Locate and identify every blood parasite.
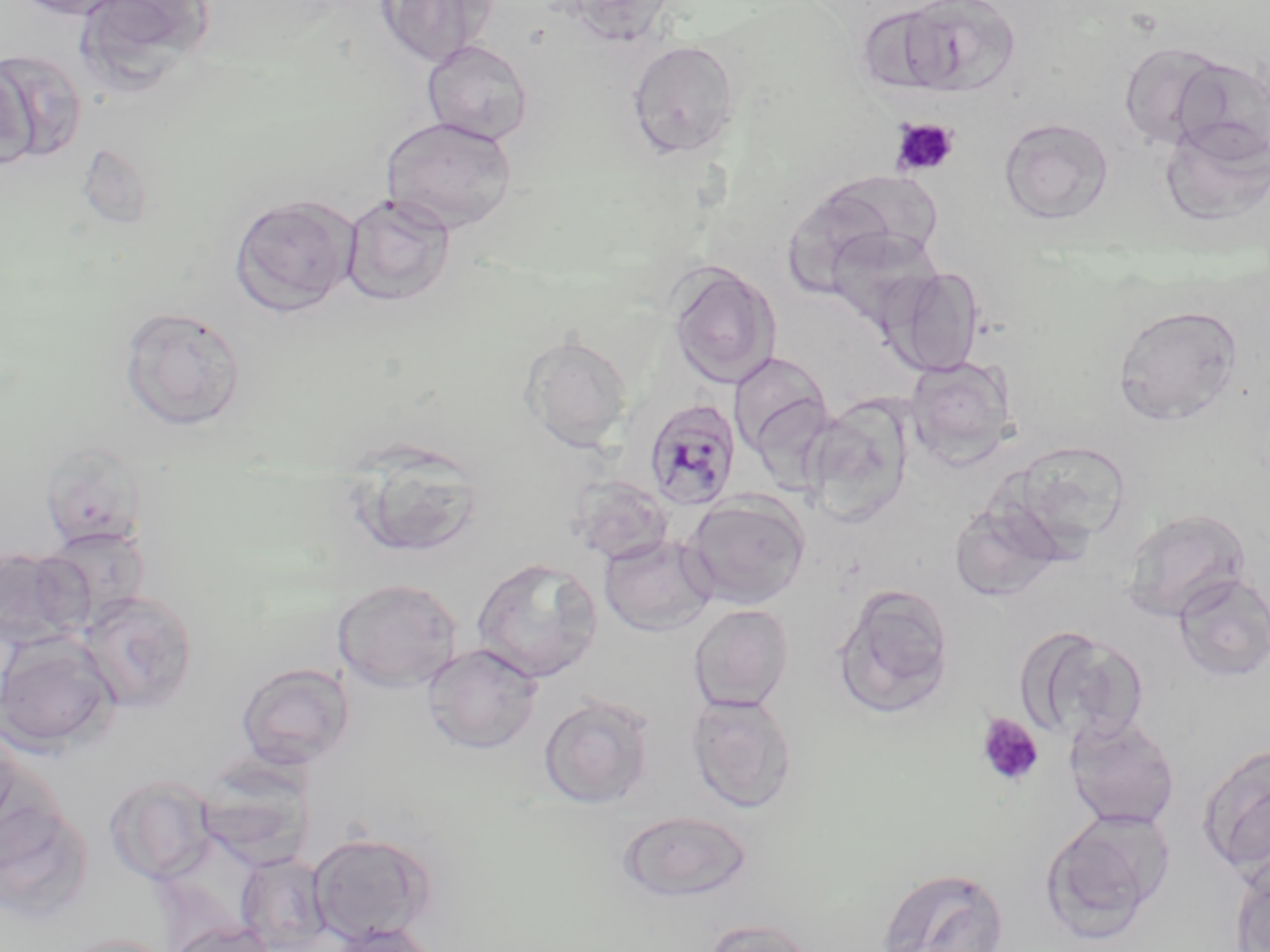
Approximate bounding boxes as [x1, y1, x2, y2] in pixels.
Plasmodium malariae-infected red blood cells: [642, 397, 742, 511].
No Plasmodium falciparum, Plasmodium ovale, Plasmodium vivax, Babesia divergens, or Trypanosoma brucei observed.

Summary:
  - Platelet locations: [891, 118, 959, 177], [976, 714, 1044, 787]
  - Uninfected red blood cell locations: [10, 0, 137, 20], [73, 0, 215, 92], [376, 0, 499, 68], [558, 0, 677, 45], [880, 0, 1022, 98], [421, 39, 533, 145], [625, 39, 742, 161], [1118, 41, 1228, 149], [0, 48, 88, 163], [1171, 55, 1270, 164], [1, 56, 37, 172], [1159, 115, 1270, 226], [380, 116, 518, 234], [998, 117, 1114, 225], [77, 144, 153, 230], [780, 178, 928, 297], [229, 192, 360, 317], [340, 193, 457, 306], [822, 226, 945, 330], [666, 261, 781, 390], [884, 265, 985, 377], [1113, 303, 1244, 427], [118, 305, 247, 430], [519, 333, 633, 451], [728, 350, 832, 464], [906, 356, 1017, 467], [803, 398, 913, 526], [1012, 440, 1133, 551], [347, 442, 488, 559], [568, 475, 674, 565], [683, 492, 810, 610], [948, 497, 1065, 603], [1121, 507, 1251, 621], [43, 525, 149, 626], [599, 533, 718, 637], [0, 546, 89, 650], [471, 557, 603, 683], [1173, 572, 1270, 683], [332, 577, 464, 693], [831, 583, 956, 719], [79, 590, 199, 713], [688, 603, 794, 713], [1019, 626, 1150, 747], [0, 630, 120, 756], [421, 643, 543, 754], [236, 662, 354, 769], [539, 692, 655, 809], [687, 693, 798, 813], [1063, 713, 1181, 831], [0, 723, 27, 840], [1197, 742, 1270, 877], [195, 764, 315, 869], [104, 775, 217, 883], [0, 798, 95, 923], [616, 809, 754, 903], [1039, 810, 1172, 943], [307, 830, 438, 945], [235, 851, 333, 951], [1230, 858, 1270, 952], [876, 866, 1010, 952], [700, 918, 817, 952], [169, 920, 275, 952], [323, 922, 441, 951], [54, 934, 177, 952]
  - Slide-level diagnosis: Plasmodium malariae
  - Image size: 1270×952 pixels
  - Magnification: 1000x
  - Modality: light microscopy
  - Preparation: thin blood smear
  - Stain: May-Grünwald-Giemsa
  - Field of view: single